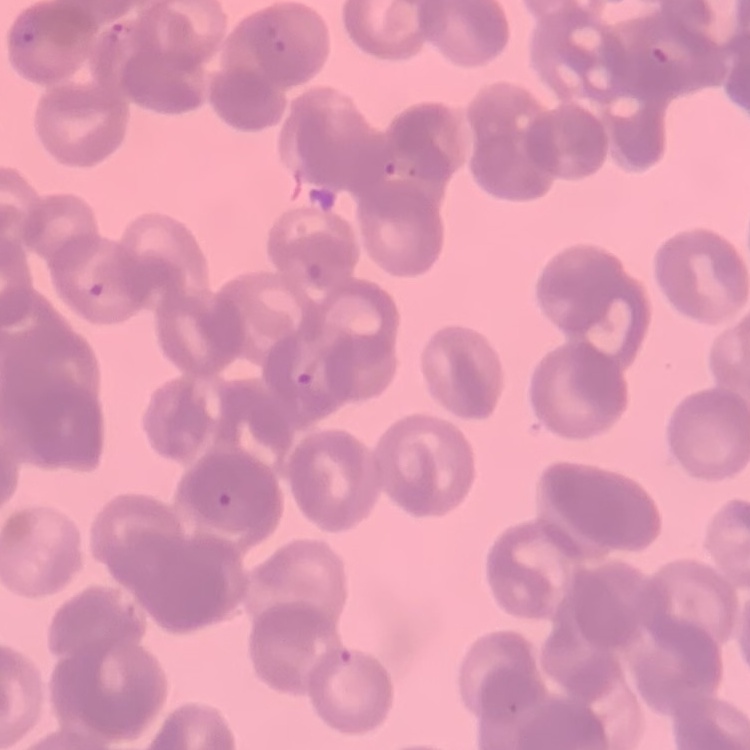
Summary:
  - Erythrocyte morphology: rouleaux formation
  - Stain: Field's or Giemsa
  - Image type: one tile cut from a larger photomicrograph
  - Preparation: thin blood film